Outline every parasitised red blood cell.
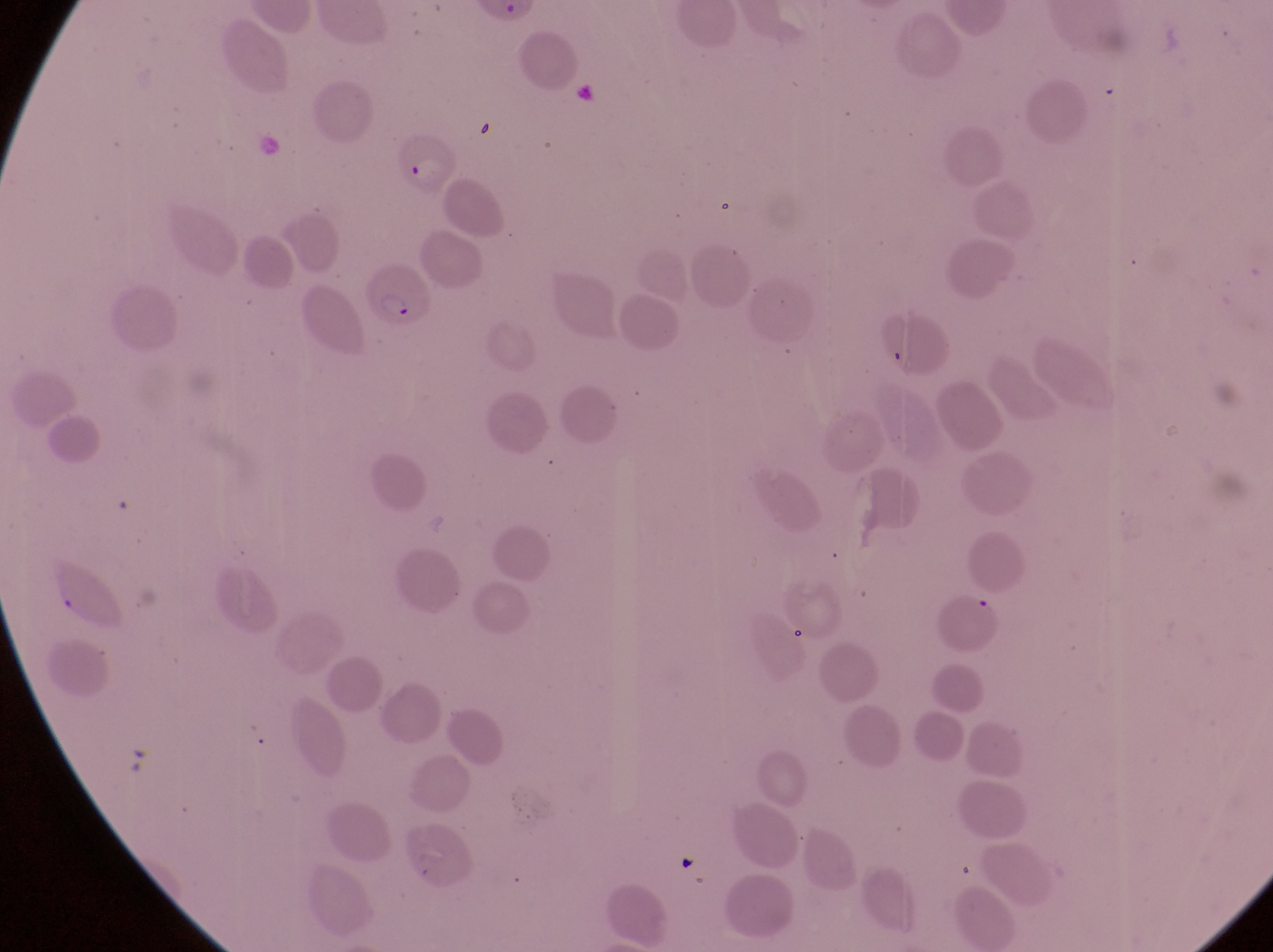

Approximate bounding boxes as [left, top, right, bottom] in pixels.
Parasitised red blood cells: [387, 128, 459, 200], [359, 265, 428, 332].

country = Uganda
capture = smartphone photograph through the eyepiece of an Olympus CX-23 microscope
image size = 1273×952 pixels
field of view = single
magnification = 1000x
preparation = thin blood film